Outline each blood parasite and name the species.
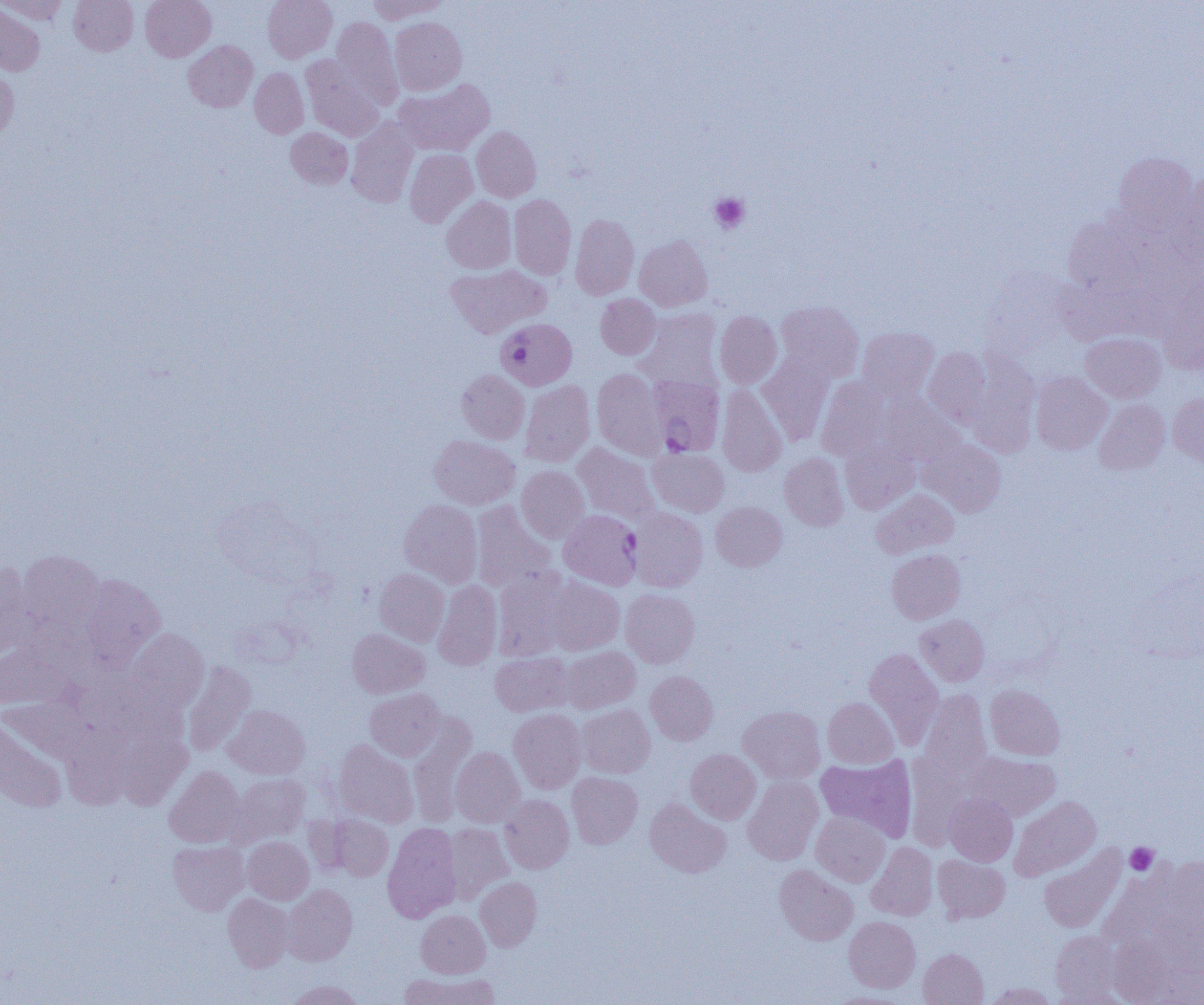
Approximate bounding boxes as named x1/y1/x2/y2 corners in pixels.
Plasmodium falciparum-infected red blood cells: (x1=496, y1=318, x2=577, y2=391), (x1=653, y1=380, x2=722, y2=462), (x1=560, y1=510, x2=647, y2=592).
No Plasmodium ovale, Plasmodium malariae, Plasmodium vivax, Babesia divergens, or Trypanosoma brucei observed.

Platelet locations: (x1=710, y1=193, x2=749, y2=233), (x1=1125, y1=843, x2=1159, y2=875). Uninfected red blood cell locations: (x1=1, y1=0, x2=69, y2=24), (x1=69, y1=0, x2=138, y2=55), (x1=140, y1=0, x2=215, y2=61), (x1=263, y1=0, x2=337, y2=62), (x1=368, y1=0, x2=447, y2=23), (x1=0, y1=3, x2=45, y2=76), (x1=332, y1=17, x2=402, y2=108), (x1=390, y1=17, x2=466, y2=95), (x1=184, y1=40, x2=258, y2=112), (x1=301, y1=56, x2=383, y2=141), (x1=250, y1=67, x2=309, y2=138), (x1=0, y1=68, x2=18, y2=142), (x1=394, y1=79, x2=495, y2=156), (x1=346, y1=119, x2=418, y2=208), (x1=286, y1=127, x2=353, y2=188), (x1=472, y1=127, x2=541, y2=201), (x1=404, y1=148, x2=477, y2=227), (x1=1111, y1=152, x2=1198, y2=232), (x1=1176, y1=172, x2=1204, y2=275), (x1=509, y1=194, x2=576, y2=280), (x1=441, y1=196, x2=516, y2=273), (x1=570, y1=214, x2=639, y2=300), (x1=634, y1=235, x2=712, y2=311), (x1=445, y1=264, x2=550, y2=338), (x1=1157, y1=280, x2=1204, y2=375), (x1=596, y1=294, x2=661, y2=359), (x1=775, y1=301, x2=864, y2=383), (x1=635, y1=309, x2=721, y2=389), (x1=715, y1=312, x2=782, y2=388), (x1=857, y1=326, x2=939, y2=402), (x1=1080, y1=332, x2=1167, y2=403), (x1=923, y1=347, x2=994, y2=428), (x1=964, y1=350, x2=1041, y2=457), (x1=758, y1=356, x2=834, y2=446), (x1=592, y1=368, x2=668, y2=459), (x1=456, y1=369, x2=529, y2=443), (x1=1030, y1=372, x2=1112, y2=455), (x1=816, y1=376, x2=891, y2=461), (x1=520, y1=380, x2=595, y2=466), (x1=717, y1=384, x2=787, y2=477), (x1=1168, y1=391, x2=1204, y2=466), (x1=880, y1=394, x2=965, y2=466), (x1=1094, y1=399, x2=1170, y2=476), (x1=428, y1=435, x2=520, y2=509), (x1=919, y1=437, x2=1006, y2=516), (x1=840, y1=439, x2=920, y2=514), (x1=573, y1=443, x2=661, y2=523), (x1=648, y1=448, x2=729, y2=516), (x1=779, y1=452, x2=849, y2=530), (x1=517, y1=465, x2=589, y2=543), (x1=871, y1=489, x2=958, y2=559), (x1=399, y1=499, x2=482, y2=588), (x1=472, y1=501, x2=557, y2=593), (x1=711, y1=501, x2=787, y2=571), (x1=628, y1=507, x2=708, y2=592), (x1=18, y1=549, x2=105, y2=640), (x1=887, y1=549, x2=965, y2=623), (x1=0, y1=562, x2=36, y2=659), (x1=375, y1=568, x2=450, y2=646), (x1=493, y1=568, x2=575, y2=660), (x1=76, y1=573, x2=165, y2=670), (x1=542, y1=574, x2=625, y2=656), (x1=433, y1=580, x2=502, y2=670), (x1=620, y1=589, x2=699, y2=668), (x1=915, y1=615, x2=989, y2=686), (x1=348, y1=628, x2=429, y2=698), (x1=127, y1=629, x2=209, y2=715), (x1=561, y1=646, x2=640, y2=713), (x1=0, y1=647, x2=73, y2=710), (x1=864, y1=648, x2=943, y2=749), (x1=490, y1=652, x2=575, y2=716), (x1=182, y1=661, x2=256, y2=756), (x1=645, y1=671, x2=718, y2=744), (x1=985, y1=685, x2=1065, y2=760), (x1=365, y1=688, x2=445, y2=761), (x1=920, y1=690, x2=991, y2=780), (x1=823, y1=697, x2=898, y2=768), (x1=576, y1=704, x2=655, y2=778), (x1=224, y1=705, x2=310, y2=779), (x1=738, y1=705, x2=825, y2=783), (x1=509, y1=708, x2=587, y2=793), (x1=408, y1=714, x2=477, y2=826), (x1=0, y1=715, x2=68, y2=812), (x1=62, y1=723, x2=132, y2=810), (x1=118, y1=730, x2=192, y2=811), (x1=334, y1=739, x2=418, y2=827), (x1=451, y1=747, x2=525, y2=827), (x1=685, y1=749, x2=760, y2=824), (x1=906, y1=752, x2=971, y2=849), (x1=966, y1=753, x2=1060, y2=821), (x1=815, y1=754, x2=917, y2=841), (x1=165, y1=766, x2=245, y2=848), (x1=567, y1=771, x2=642, y2=848), (x1=231, y1=774, x2=310, y2=844), (x1=743, y1=776, x2=823, y2=865), (x1=945, y1=794, x2=1017, y2=866), (x1=499, y1=795, x2=574, y2=873), (x1=1010, y1=796, x2=1100, y2=880), (x1=645, y1=798, x2=731, y2=878), (x1=811, y1=811, x2=890, y2=886), (x1=329, y1=816, x2=393, y2=881), (x1=382, y1=822, x2=461, y2=922), (x1=443, y1=823, x2=513, y2=902), (x1=242, y1=837, x2=314, y2=904), (x1=168, y1=840, x2=249, y2=914), (x1=866, y1=842, x2=938, y2=920), (x1=1039, y1=844, x2=1127, y2=934), (x1=933, y1=855, x2=1010, y2=923), (x1=775, y1=864, x2=858, y2=945), (x1=475, y1=877, x2=542, y2=951), (x1=282, y1=884, x2=357, y2=966), (x1=223, y1=893, x2=294, y2=972), (x1=416, y1=909, x2=490, y2=978), (x1=844, y1=916, x2=920, y2=993), (x1=1050, y1=931, x2=1121, y2=1003), (x1=918, y1=948, x2=988, y2=1005), (x1=399, y1=972, x2=498, y2=1005), (x1=287, y1=980, x2=364, y2=1005), (x1=985, y1=982, x2=1057, y2=1004), (x1=828, y1=991, x2=912, y2=1004). Slide-level diagnosis: Plasmodium falciparum. Single field of view. 1000x magnification. Optical microscopy. Image is 1204×1005 pixels. Thin blood film.